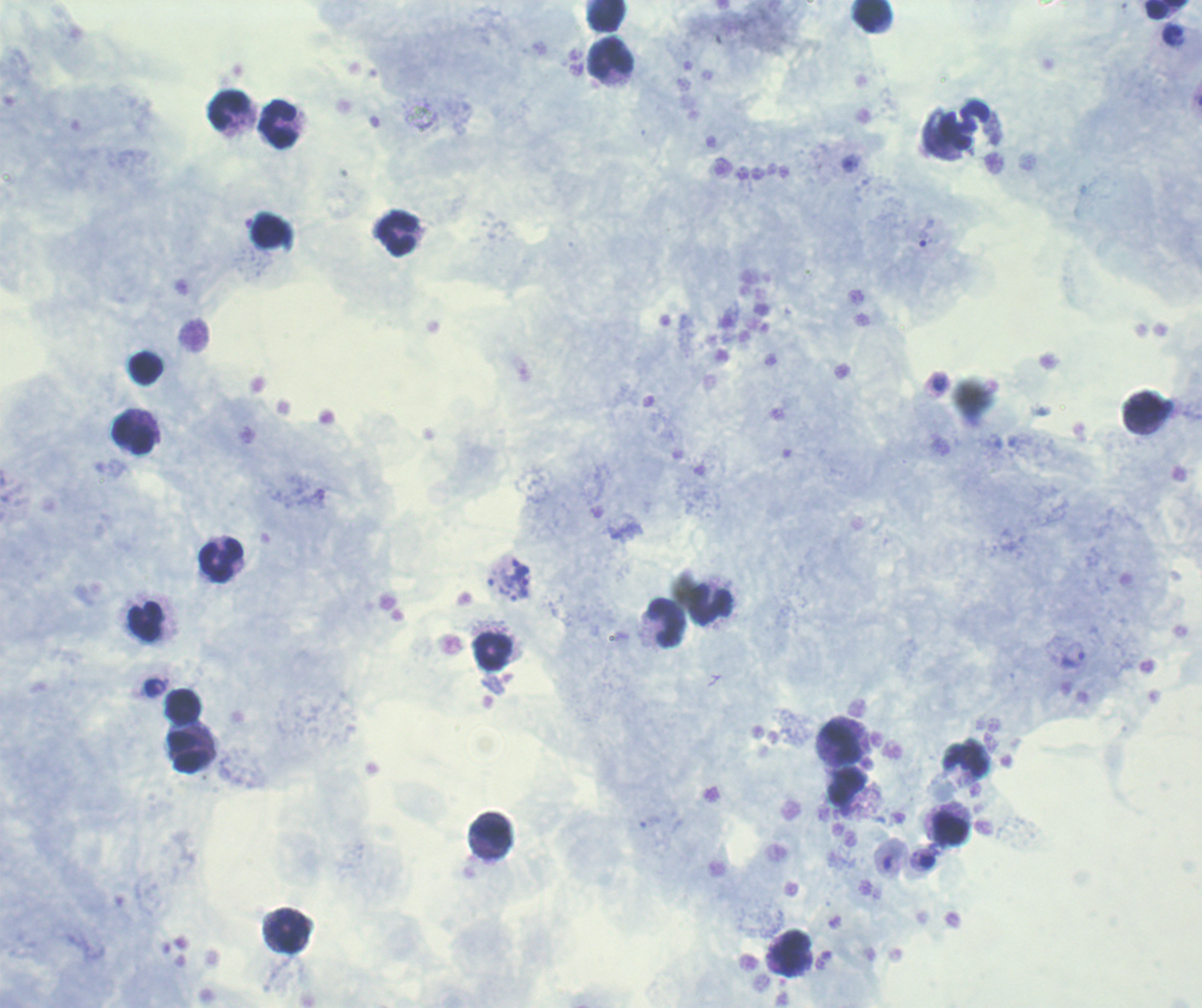
Approximate centers as [x, y] in pixels.
Summary:
  - Leukocyte locations: [1167, 9], [873, 15], [607, 16], [611, 59], [229, 111], [279, 124], [397, 235], [145, 369], [1147, 412], [134, 435], [221, 562], [711, 605], [145, 623], [667, 623], [494, 653], [184, 707], [843, 744], [189, 752], [950, 828], [491, 833], [292, 932], [793, 954]
  - Trophozoite locations: [518, 569], [523, 589]
  - Result: malaria parasites identified
  - Coloration quality: good
  - Stain: Romanowsky
  - Image size: 1202×1008 pixels
  - Context: previously used in an actual diagnosis
  - Field of view: single
  - Preparation: thick blood film
  - Magnification: 100x
  - Background quality: good